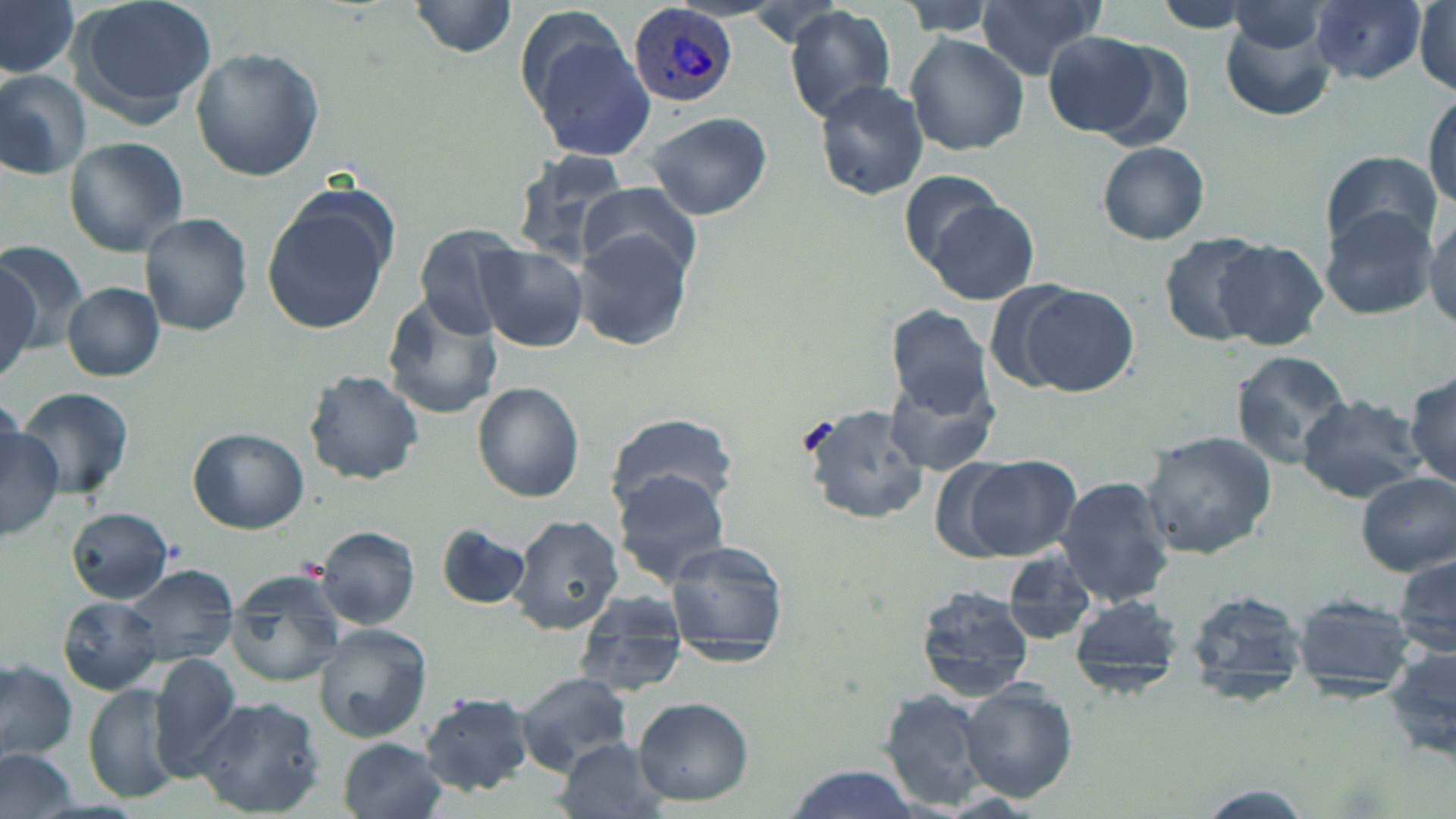

Summary:
  - Coordinate format: approximate bounding boxes as [x1, y1, x2, y2] in pixels
  - Plasmodium vivax-infected red blood cell locations: [628, 4, 738, 107]
  - Uninfected red blood cell locations: [69, 0, 217, 122], [409, 0, 520, 56], [899, 0, 1005, 34], [975, 0, 1103, 78], [1152, 0, 1257, 33], [1312, 0, 1426, 85], [0, 1, 79, 77], [1414, 1, 1453, 96], [1230, 4, 1331, 53], [782, 5, 898, 123], [1217, 6, 1339, 117], [526, 27, 658, 161], [1044, 30, 1162, 137], [905, 32, 1030, 157], [190, 48, 325, 182], [0, 70, 91, 179], [815, 80, 931, 200], [1426, 89, 1456, 209], [648, 111, 771, 220], [64, 137, 189, 257], [1096, 141, 1211, 245], [1320, 150, 1443, 254], [510, 152, 634, 270], [899, 170, 1008, 268], [578, 186, 699, 281], [261, 195, 395, 337], [924, 199, 1039, 304], [1318, 207, 1437, 320], [1425, 210, 1456, 330], [140, 215, 253, 334], [415, 223, 528, 337], [572, 231, 696, 352], [1159, 232, 1275, 346], [1214, 241, 1330, 349], [0, 243, 62, 368], [479, 247, 587, 352], [1010, 281, 1141, 397], [62, 282, 166, 382], [379, 294, 505, 419], [885, 303, 994, 415], [1231, 350, 1353, 469], [883, 367, 1001, 476], [304, 369, 425, 484], [1404, 371, 1455, 491], [472, 382, 586, 503], [18, 386, 136, 501], [1297, 395, 1424, 501], [800, 403, 929, 526], [606, 411, 736, 518], [0, 425, 61, 539], [189, 428, 310, 534], [1140, 429, 1279, 559], [963, 455, 1081, 561], [613, 470, 733, 585], [1355, 471, 1456, 576], [1054, 476, 1177, 609], [67, 508, 175, 602], [508, 515, 623, 634], [435, 522, 532, 610], [314, 525, 420, 630], [662, 538, 791, 661], [1003, 551, 1096, 648], [1393, 551, 1454, 663], [117, 563, 238, 668], [224, 574, 348, 688], [913, 586, 1034, 704], [1185, 588, 1311, 706], [576, 592, 688, 693], [1290, 592, 1416, 701], [1069, 593, 1187, 694], [58, 599, 164, 693], [313, 624, 435, 741], [1382, 645, 1456, 765], [149, 653, 247, 778], [0, 658, 77, 764], [513, 672, 634, 771], [957, 681, 1078, 802], [84, 684, 183, 804], [875, 688, 996, 809], [421, 691, 538, 796], [191, 696, 325, 816], [633, 696, 752, 806], [338, 738, 450, 819], [556, 739, 673, 819], [0, 747, 80, 819], [780, 766, 925, 819]
  - Slide-level diagnosis: Plasmodium vivax
  - Image size: 1456×819 pixels
  - Magnification: 1000x
  - Modality: light microscopy
  - Stain: May-Grünwald-Giemsa
  - Field of view: one of a larger specimen
  - Preparation: thin blood smear